Classify this cell by malaria status.
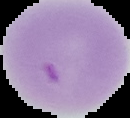

It is uninfected.

Image is 130×118 pixels. Segmented cell region on a black background. From a thin blood film.